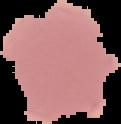 Image is 121×124 pixels. From a thin blood film. Result: negative for malaria parasites. Cell region segmented out of the field of view; the surrounding area is masked to black.